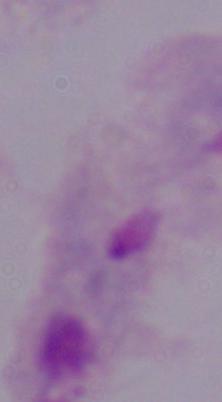

identification = trichomonad
magnification = 1000x
modality = micrograph